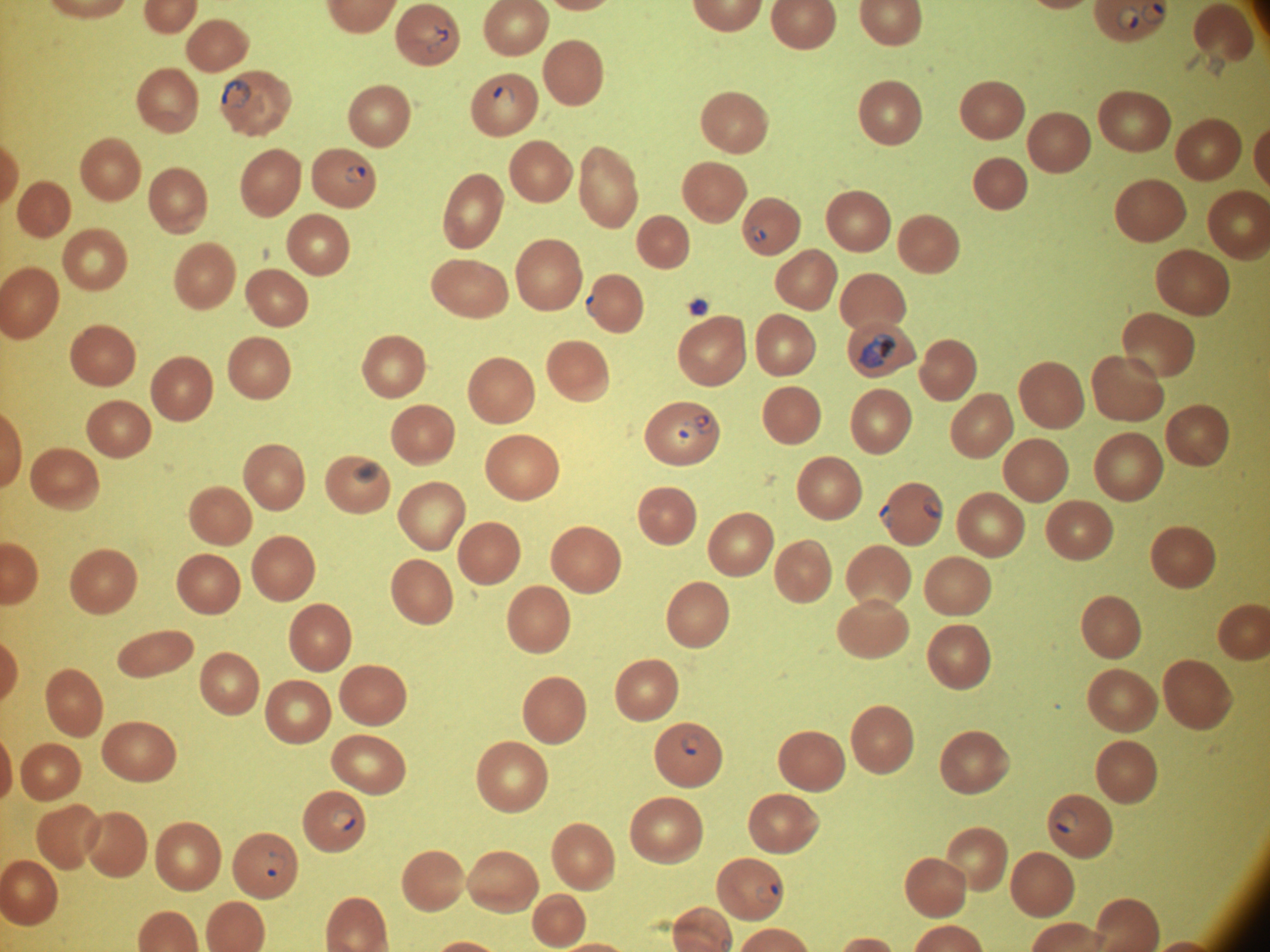
life-cycle stages among the annotated parasites = ring form, trophozoite
field of view = single
ring form locations = approximate bounding boxes as (x1, y1, x2, y2) in pixels, from the source annotation, which is not necessarily exhaustive: (1140, 1, 1166, 24), (1117, 6, 1140, 31), (434, 24, 448, 42), (221, 79, 252, 108), (493, 85, 515, 105), (345, 163, 366, 184), (751, 225, 767, 242), (586, 294, 602, 316), (693, 414, 714, 434), (671, 422, 698, 443), (924, 494, 942, 518), (879, 504, 892, 528), (681, 732, 703, 755), (333, 809, 356, 831), (1054, 809, 1079, 834), (264, 850, 289, 879), (756, 884, 779, 902)
preparation = thin blood film
species = Plasmodium falciparum
microscope = Leica DM2000 with built-in camera
magnification = 100x
stain = Giemsa
image size = 1270×952 pixels
trophozoite locations = approximate bounding boxes as (x1, y1, x2, y2) in pixels, from the source annotation, which is not necessarily exhaustive: (857, 333, 897, 369), (353, 460, 380, 483)